Outline each Plasmodium vivax-infected red blood cell.
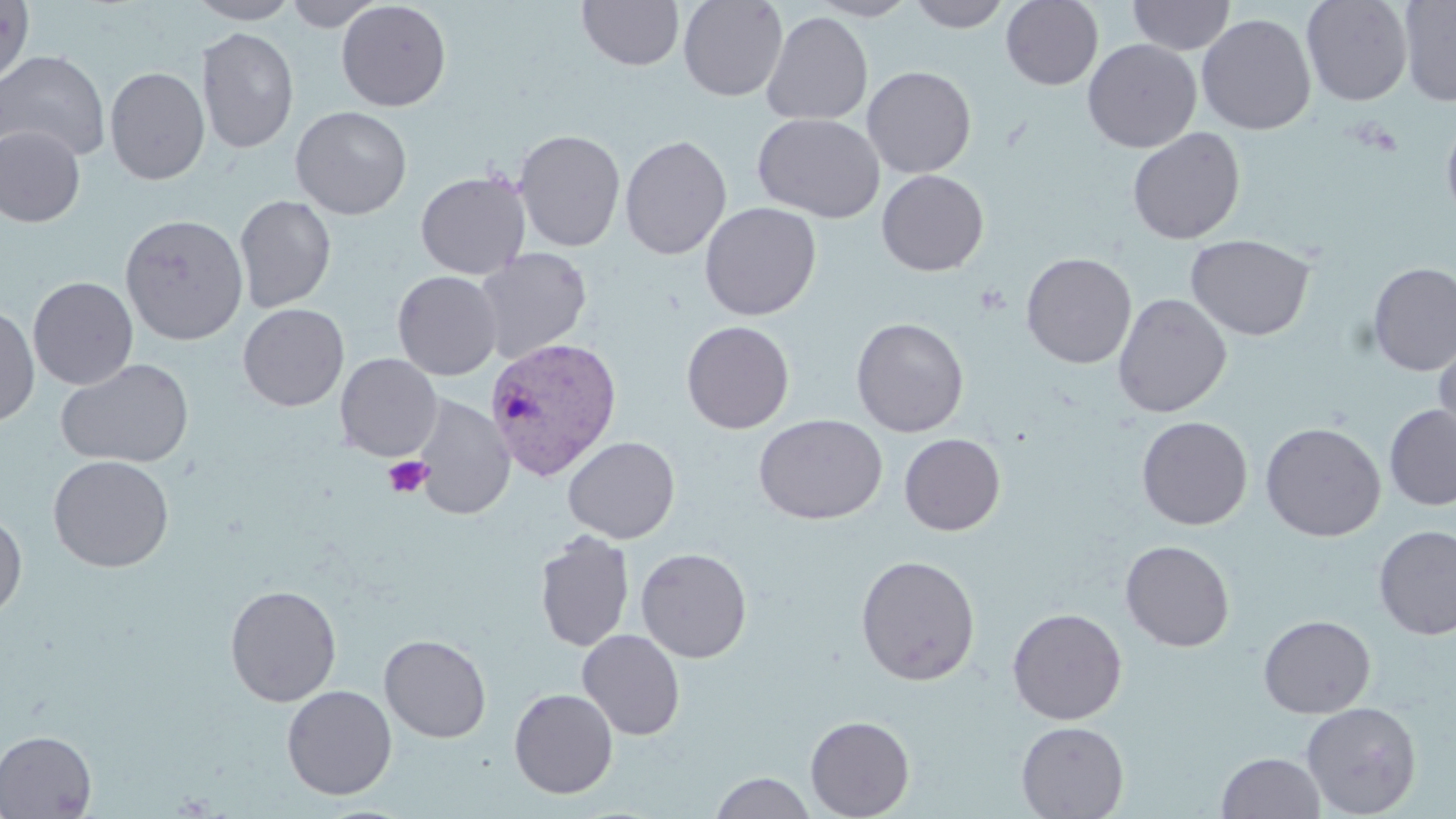
Approximate bounding boxes as [x1, y1, x2, y2] in pixels.
Plasmodium vivax-infected red blood cells: [484, 337, 622, 480].

{
  "slide_level_diagnosis": "Plasmodium vivax",
  "modality": "light microscopy",
  "platelet_locations": "approximate bounding boxes as [x1, y1, x2, y2] in pixels: [383, 455, 432, 498]",
  "image_size": "1456×819 pixels",
  "stain": "May-Grünwald-Giemsa",
  "magnification": "1000x",
  "field_of_view": "one of a larger specimen",
  "uninfected_red_blood_cell_locations": "approximate bounding boxes as [x1, y1, x2, y2] in pixels: [186, 0, 301, 24], [284, 0, 385, 31], [576, 0, 685, 72], [678, 0, 788, 101], [807, 0, 919, 21], [908, 0, 1011, 32], [1001, 0, 1103, 90], [1127, 0, 1236, 56], [1301, 0, 1414, 106], [1398, 0, 1456, 106], [0, 1, 35, 85], [336, 1, 452, 111], [761, 11, 873, 126], [1196, 13, 1316, 135], [196, 27, 299, 155], [1082, 39, 1201, 153], [0, 49, 111, 163], [105, 66, 210, 185], [862, 66, 976, 178], [290, 105, 413, 220], [752, 113, 885, 223], [1441, 115, 1456, 227], [0, 125, 85, 227], [1127, 127, 1246, 245], [514, 129, 625, 252], [619, 135, 732, 260], [876, 170, 989, 276], [415, 171, 530, 279], [234, 195, 336, 313], [699, 202, 822, 321], [120, 214, 249, 346], [1186, 234, 1315, 341], [474, 248, 592, 364], [1021, 252, 1137, 369], [1367, 261, 1456, 376], [392, 271, 503, 380], [28, 276, 138, 390], [1113, 293, 1232, 418], [238, 303, 349, 411], [0, 304, 39, 428], [850, 317, 969, 437], [681, 321, 795, 433], [1433, 336, 1456, 449], [335, 353, 442, 461], [55, 358, 194, 469], [412, 395, 515, 521], [1384, 404, 1456, 511], [753, 414, 887, 524], [1136, 416, 1252, 530], [1260, 422, 1386, 541], [899, 433, 1005, 535], [562, 436, 680, 544], [48, 454, 174, 573], [0, 511, 27, 620], [1373, 525, 1456, 641], [534, 530, 635, 653], [1120, 540, 1235, 652], [635, 547, 752, 663], [855, 554, 980, 686], [225, 584, 341, 707], [1007, 607, 1127, 725], [1258, 614, 1375, 718], [577, 629, 686, 740], [379, 634, 491, 743], [282, 685, 397, 800], [509, 688, 618, 798], [1301, 701, 1422, 818], [805, 715, 915, 819], [1015, 721, 1129, 819], [0, 730, 97, 818], [1216, 751, 1326, 819], [711, 771, 816, 819]",
  "preparation": "thin blood smear"
}